Report the malaria status of this cell.
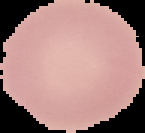

It is uninfected.

Image is 145×133 pixels. Segmented cell region on a black background. From a thin blood film.